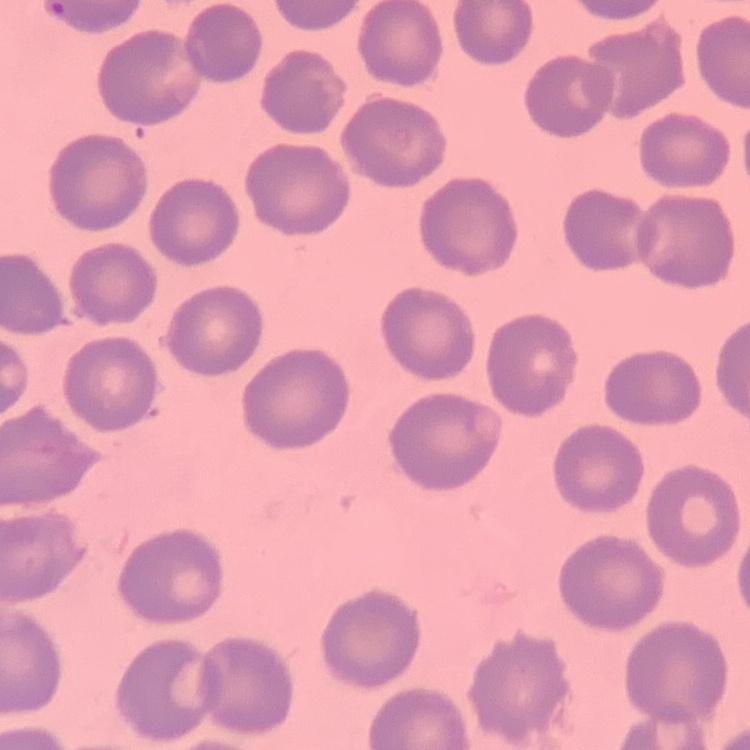

The erythrocytes show no rouleaux formation. Stained with either Field's or Giemsa. Thin peripheral smear. Square crop of a larger photomicrograph.